Comment on the morphology of the red blood cells.
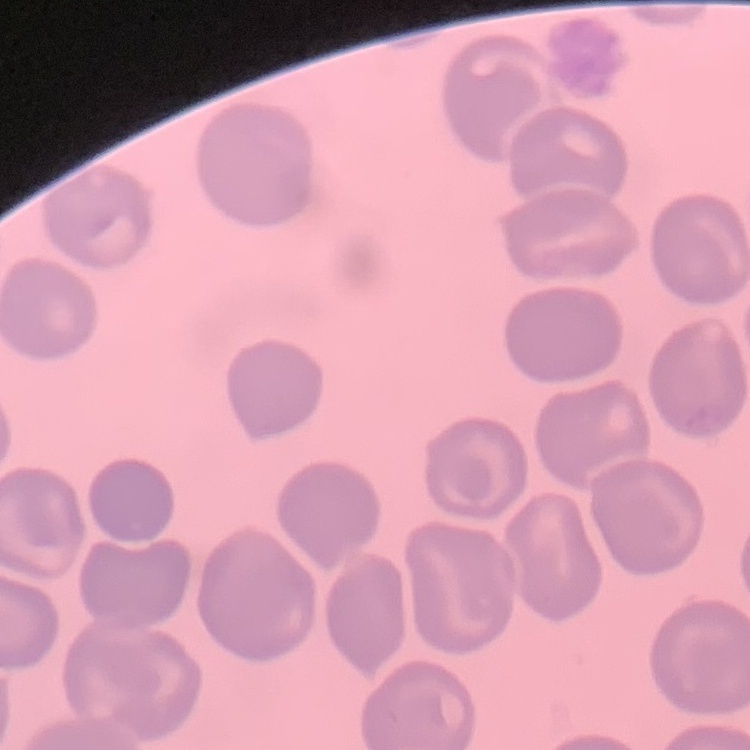

No rouleaux formation.

preparation = thin blood film
image type = square crop of a larger photomicrograph
stain = Field's or Giemsa